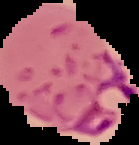
Image is 139×145 pixels. From a thin blood film. Result: Plasmodium parasites identified. Segmented cell region on a black background.